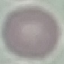

Summary:
  - Result: no malaria parasites seen
  - Capture: smartphone camera at the microscope eyepiece
  - Preparation: thin smear
  - Stain: Giemsa
  - Image type: cell patch, automatically extracted from a larger field of view and resized to 64 × 64 pixels